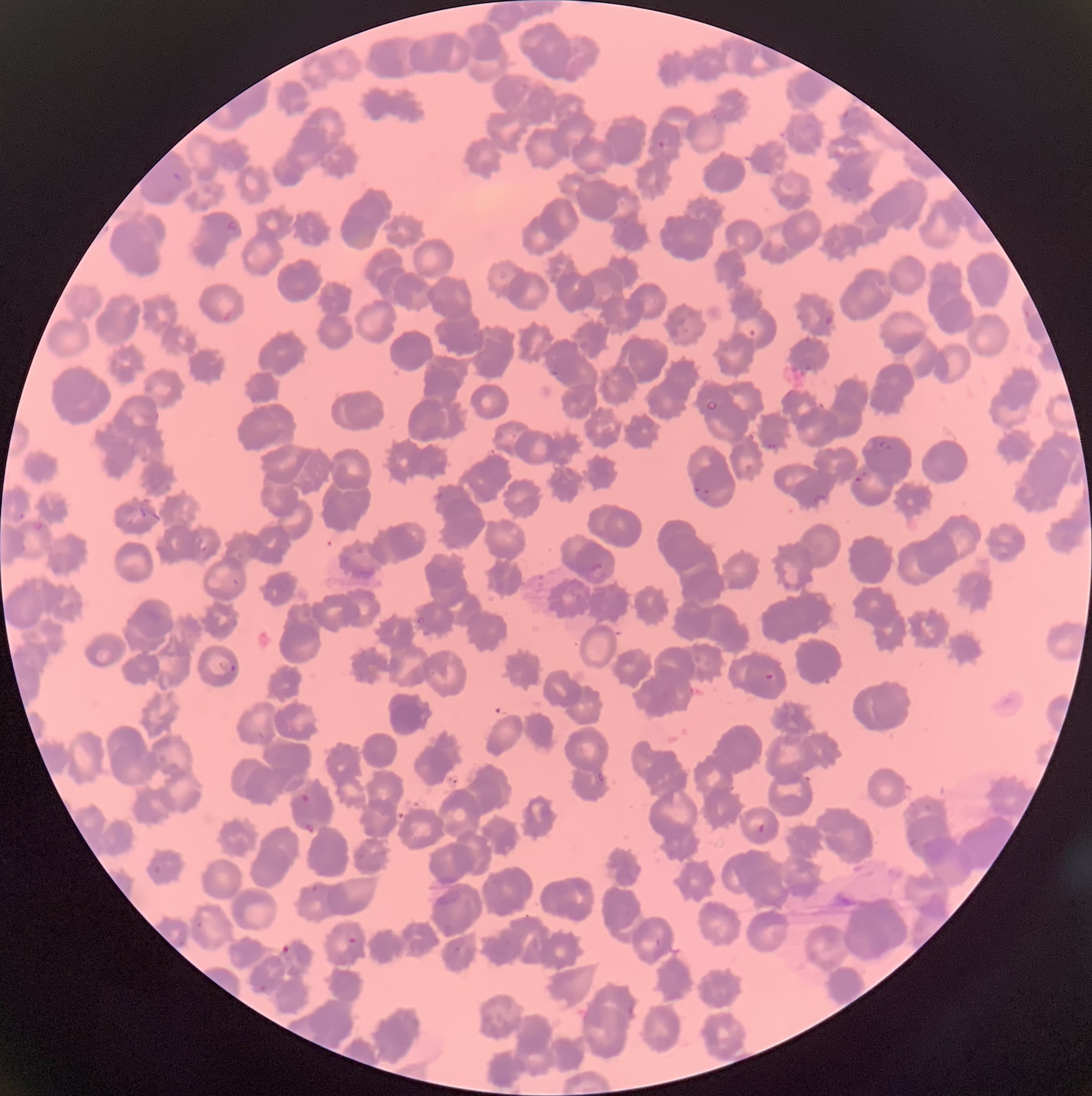

coordinate format = approximate bounding boxes as named x1/y1/x2/y2 corners in pixels
Plasmodium parasite locations = (x1=842, y1=109, x2=857, y2=127), (x1=657, y1=139, x2=667, y2=149), (x1=171, y1=171, x2=185, y2=184), (x1=224, y1=219, x2=238, y2=234), (x1=823, y1=315, x2=833, y2=326), (x1=748, y1=328, x2=756, y2=336), (x1=804, y1=363, x2=814, y2=372), (x1=548, y1=367, x2=561, y2=379), (x1=875, y1=440, x2=890, y2=456), (x1=765, y1=441, x2=779, y2=450), (x1=861, y1=466, x2=871, y2=475), (x1=853, y1=476, x2=862, y2=483), (x1=694, y1=484, x2=711, y2=503), (x1=437, y1=490, x2=444, y2=500), (x1=14, y1=512, x2=25, y2=524), (x1=29, y1=520, x2=45, y2=533), (x1=588, y1=562, x2=607, y2=582), (x1=218, y1=660, x2=237, y2=673), (x1=765, y1=672, x2=777, y2=680), (x1=299, y1=793, x2=310, y2=804), (x1=303, y1=820, x2=317, y2=834), (x1=756, y1=823, x2=766, y2=834), (x1=150, y1=865, x2=161, y2=878), (x1=311, y1=885, x2=320, y2=893), (x1=194, y1=922, x2=204, y2=929), (x1=347, y1=936, x2=358, y2=945), (x1=177, y1=940, x2=186, y2=949), (x1=281, y1=943, x2=293, y2=956), (x1=253, y1=983, x2=269, y2=993)
preparation = thin blood film
red blood cell morphology = rouleaux formation
image size = 1092×1096 pixels
modality = light microscopy